Classify this cell by malaria status.
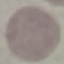
It is uninfected.

{
  "preparation": "thin blood smear",
  "stain": "Giemsa",
  "capture": "smartphone through the microscope eyepiece",
  "image_type": "automatically extracted cell patch, resized to 64 × 64 pixels"
}